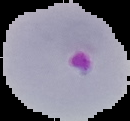
Summary:
  - Image size: 130×121 pixels
  - Preparation: thin blood smear
  - Image type: segmented cell region with the area outside set to black
  - Result: malaria parasites detected